Assess this cell for malaria.
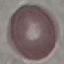

Uninfected.

Automatically extracted cell patch, resized to 64 × 64 pixels. Acquired by smartphone through the microscope eyepiece. Thin blood film. Giemsa stain.